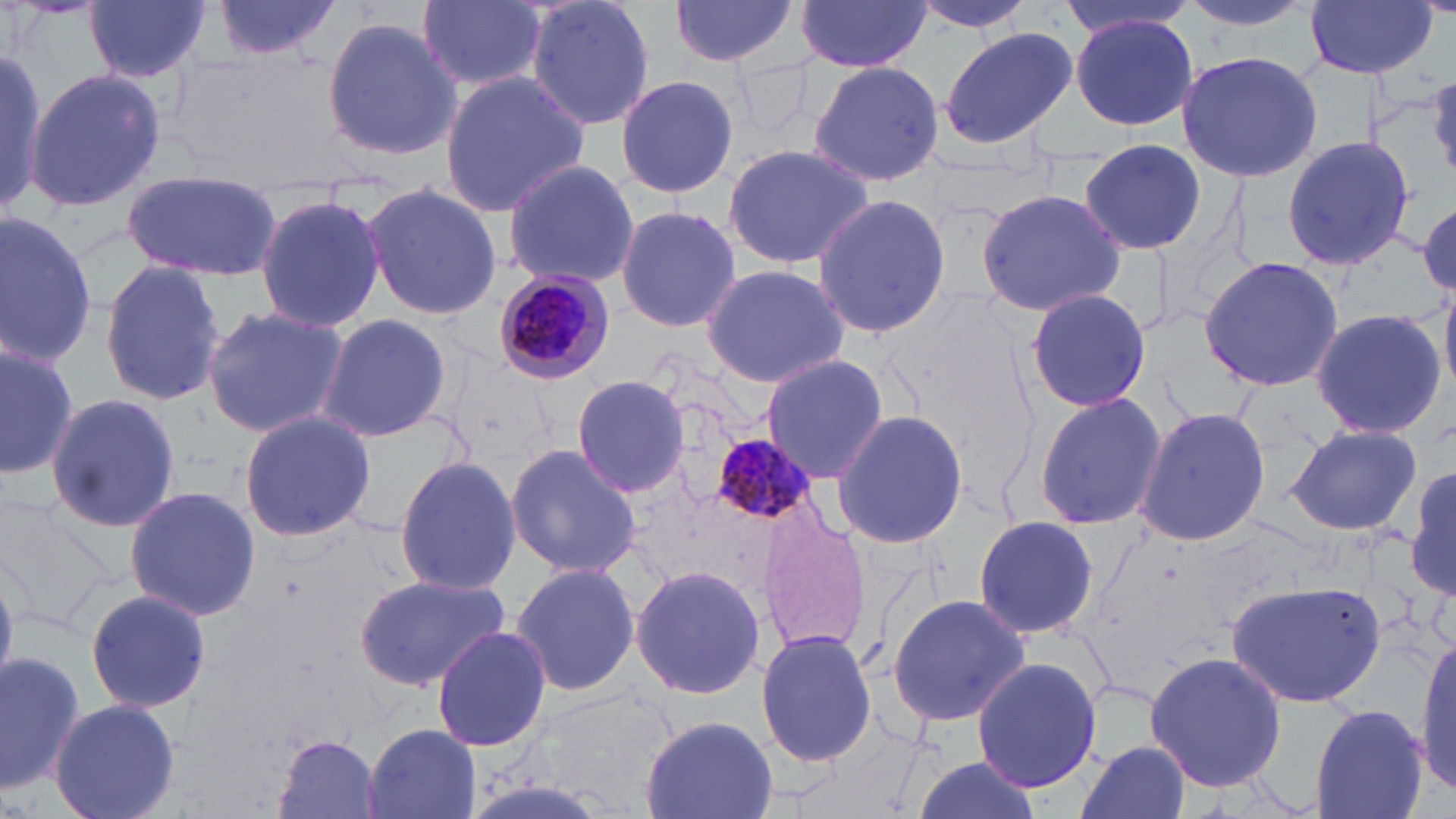
slide_level_diagnosis: Plasmodium malariae
stain: May-Grünwald-Giemsa
plasmodium_malariae_infected_red_blood_cell_locations: 'approximate bounding boxes as [x1, y1, x2, y2] in pixels: [490, 269, 616, 387], [711, 431, 817, 527]'
field_of_view: single
preparation: thin blood film
magnification: 1000x
image_size: 1456×819 pixels
uninfected_red_blood_cell_locations: 'approximate bounding boxes as [x1, y1, x2, y2] in pixels: [86, 0, 210, 84], [212, 0, 341, 61], [524, 0, 657, 134], [668, 0, 803, 67], [907, 0, 1040, 32], [1050, 0, 1194, 38], [1175, 0, 1323, 34], [1302, 0, 1439, 79], [796, 1, 932, 72], [414, 2, 548, 94], [1070, 14, 1199, 131], [322, 15, 462, 162], [937, 26, 1082, 152], [1176, 50, 1322, 183], [0, 55, 58, 213], [808, 60, 946, 189], [26, 67, 165, 213], [439, 72, 590, 216], [1427, 74, 1456, 179], [614, 75, 741, 200], [1279, 132, 1417, 272], [1077, 137, 1208, 256], [720, 142, 877, 273], [500, 158, 638, 286], [123, 171, 282, 280], [359, 180, 505, 323], [975, 185, 1127, 318], [811, 193, 952, 338], [254, 194, 386, 333], [1417, 199, 1455, 295], [615, 204, 741, 335], [0, 212, 100, 368], [1199, 255, 1344, 394], [99, 262, 226, 403], [698, 263, 850, 388], [1023, 286, 1154, 415], [200, 305, 347, 436], [1308, 308, 1449, 438], [316, 312, 452, 443], [0, 339, 77, 475], [758, 354, 889, 485], [571, 374, 690, 499], [1031, 388, 1169, 535], [44, 392, 181, 536], [1133, 406, 1272, 547], [831, 409, 969, 549], [237, 411, 376, 541], [1284, 423, 1422, 536], [505, 443, 641, 578], [394, 455, 520, 597], [1407, 459, 1456, 604], [123, 485, 261, 623], [0, 501, 119, 628], [756, 506, 873, 657], [972, 514, 1099, 641], [511, 560, 640, 699], [630, 564, 768, 700], [354, 570, 512, 692], [1226, 578, 1386, 711], [84, 588, 212, 716], [885, 593, 1031, 726], [430, 625, 553, 752], [756, 628, 877, 767], [1413, 629, 1456, 799], [0, 648, 86, 795], [1144, 651, 1286, 795], [971, 657, 1102, 794], [530, 687, 680, 810], [49, 698, 181, 819], [1309, 704, 1430, 819], [640, 714, 779, 819], [363, 725, 482, 819], [273, 735, 383, 817], [1074, 740, 1193, 819], [902, 754, 1046, 819]'
modality: light microscopy